Point out each Plasmodium parasite and classify it by life-cycle stage.
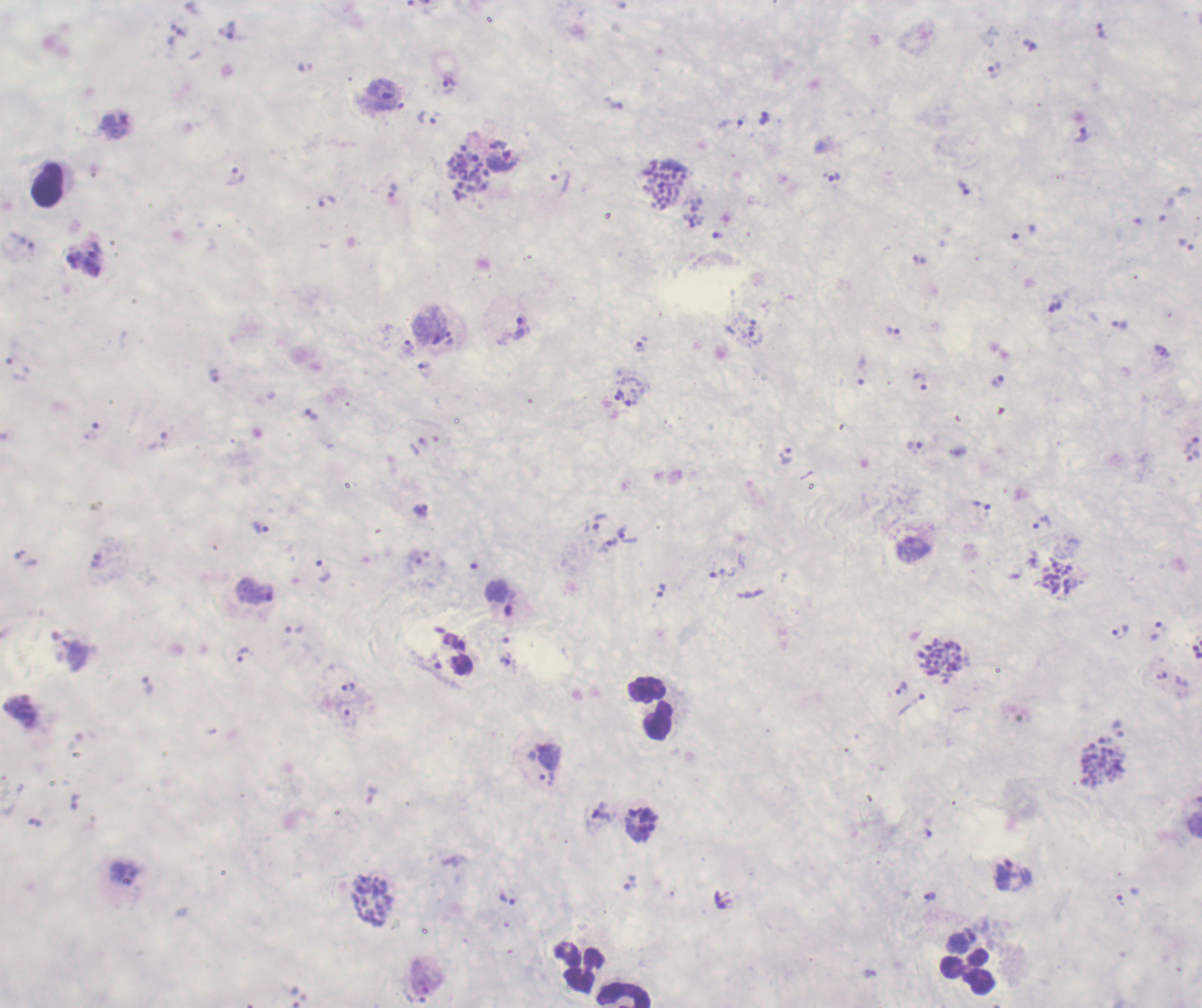

Approximate object centers, in pixels from the top-left corner.
Trophozoites: (x=1100, y=31), (x=994, y=71), (x=448, y=82), (x=384, y=89), (x=764, y=118), (x=428, y=119), (x=731, y=123), (x=115, y=126), (x=1082, y=134), (x=502, y=159), (x=236, y=175), (x=832, y=176), (x=964, y=188), (x=328, y=200), (x=694, y=222), (x=1055, y=307), (x=753, y=324), (x=1119, y=325), (x=519, y=327), (x=892, y=331), (x=755, y=337), (x=449, y=338), (x=640, y=344), (x=408, y=347), (x=423, y=368), (x=861, y=371), (x=920, y=382), (x=997, y=382), (x=618, y=395), (x=312, y=414), (x=1192, y=444), (x=914, y=446), (x=785, y=455), (x=1193, y=456), (x=982, y=505), (x=599, y=521), (x=1042, y=523), (x=261, y=528), (x=628, y=535), (x=609, y=545), (x=323, y=570), (x=722, y=573), (x=255, y=592), (x=499, y=598), (x=1119, y=633), (x=242, y=655), (x=507, y=659), (x=461, y=665), (x=348, y=686), (x=901, y=687), (x=1119, y=729), (x=1004, y=874), (x=930, y=897), (x=507, y=899).
Schizonts: (x=470, y=173), (x=666, y=186), (x=1059, y=577), (x=943, y=660), (x=1103, y=763), (x=372, y=901).
No gametocyte forms observed.

Approximate object centers, in pixels from the top-left corner. Leukocyte locations: (x=48, y=185), (x=650, y=709), (x=578, y=968), (x=967, y=973), (x=625, y=996). Background quality: poor. Thick blood smear. Previously used in an actual diagnosis. Captured at 100x magnification. Single field of view. Image is 1202×1008 pixels. Romanowsky-stained preparation. Coloration quality: bad.